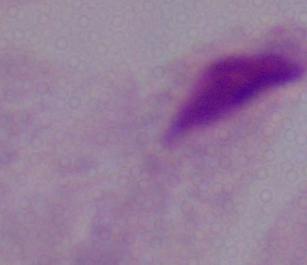

Summary:
  - Identification: trichomonad
  - Modality: micrograph
  - Magnification: 1000x